Identify the blood parasite species.
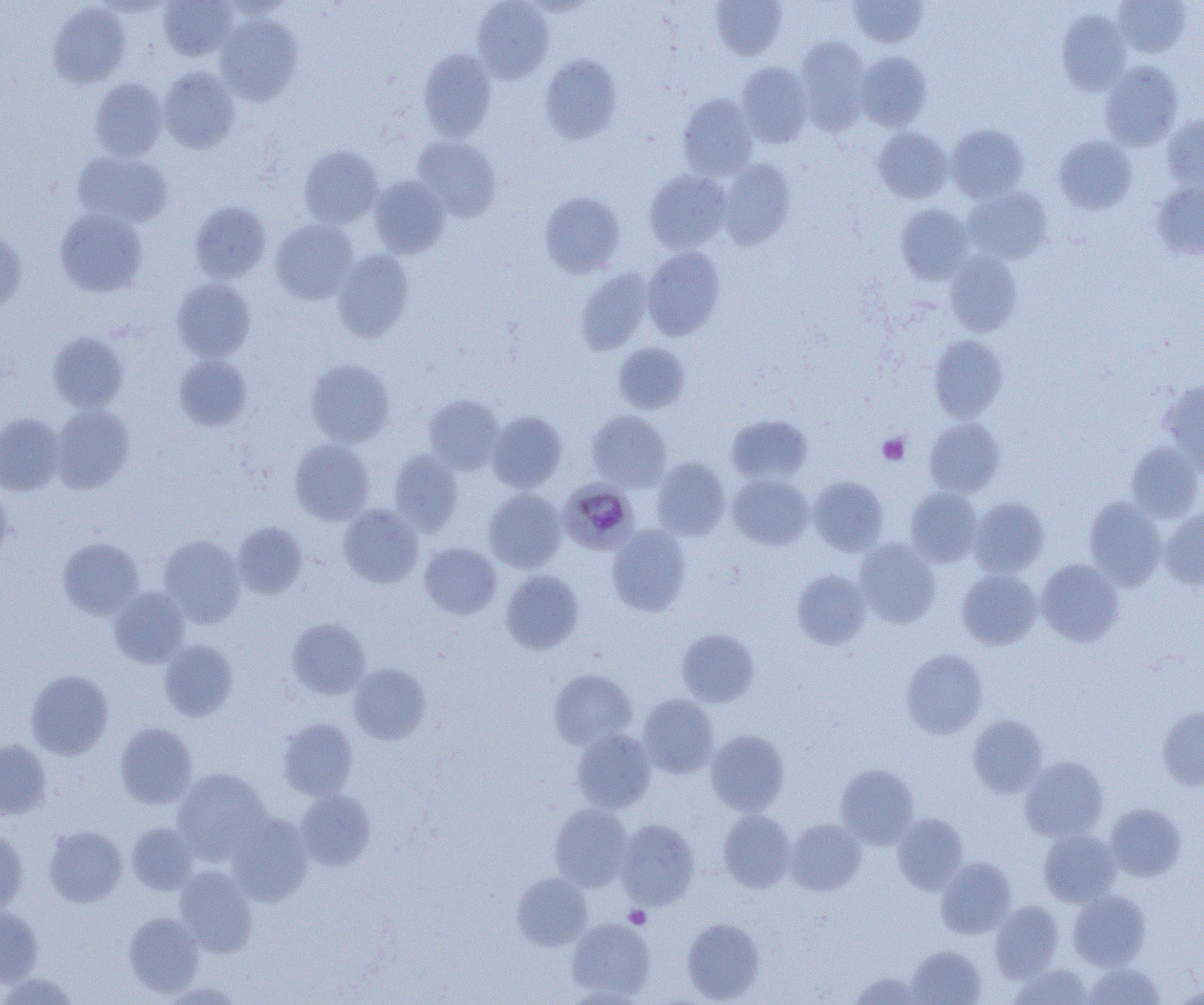

Plasmodium malariae.

Summary:
  - Coordinate format: approximate bounding boxes as (x1, y1, x2, y2) in pixels
  - Platelet locations: (877, 433, 909, 465), (624, 906, 650, 929)
  - Plasmodium malariae-infected red blood cell locations: (558, 480, 638, 554)
  - Uninfected red blood cell locations: (158, 0, 237, 61), (711, 0, 788, 60), (849, 0, 929, 48), (1111, 0, 1192, 58), (472, 1, 554, 83), (48, 3, 131, 89), (1057, 10, 1131, 95), (215, 14, 303, 104), (794, 37, 870, 135), (418, 48, 496, 141), (855, 51, 932, 131), (539, 54, 622, 144), (1100, 60, 1183, 150), (736, 62, 813, 147), (159, 68, 240, 153), (90, 78, 167, 161), (678, 93, 759, 180), (1162, 115, 1204, 191), (946, 123, 1029, 203), (872, 126, 952, 203), (1054, 135, 1137, 214), (411, 136, 502, 221), (299, 145, 383, 228), (73, 151, 173, 227), (719, 159, 796, 249), (644, 168, 732, 253), (369, 176, 450, 258), (1150, 181, 1204, 261), (963, 186, 1052, 264), (538, 191, 626, 278), (189, 200, 271, 283), (896, 203, 973, 283), (54, 208, 147, 296), (270, 219, 359, 304), (0, 228, 27, 313), (641, 246, 725, 340), (333, 250, 414, 342), (944, 251, 1023, 336), (575, 269, 652, 355), (171, 278, 256, 362), (48, 332, 128, 413), (929, 335, 1008, 422), (614, 342, 690, 414), (174, 355, 252, 431), (305, 359, 395, 447), (1160, 379, 1204, 475), (424, 393, 503, 473), (51, 404, 134, 493), (587, 410, 671, 490), (486, 411, 568, 492), (0, 413, 65, 496), (726, 414, 813, 485), (925, 418, 1004, 496), (289, 439, 375, 525), (1126, 441, 1204, 522), (389, 450, 462, 535), (651, 458, 730, 540), (727, 474, 813, 550), (808, 476, 889, 556), (0, 483, 13, 566), (905, 487, 983, 566), (484, 488, 566, 572), (1084, 496, 1167, 589), (968, 497, 1049, 577), (338, 504, 423, 587), (1160, 506, 1204, 591), (232, 522, 307, 597), (607, 525, 692, 616), (158, 535, 245, 627), (58, 537, 143, 619), (854, 538, 940, 628), (420, 543, 501, 619), (1036, 558, 1124, 646), (792, 568, 871, 649), (957, 569, 1042, 650), (500, 570, 584, 655), (109, 587, 190, 667), (286, 618, 371, 699), (677, 629, 759, 706), (159, 640, 238, 721), (901, 648, 988, 738), (349, 663, 431, 744), (549, 668, 637, 750), (26, 670, 113, 760), (638, 694, 718, 778), (1157, 706, 1204, 790), (967, 714, 1048, 797), (278, 718, 358, 800), (115, 722, 198, 808), (571, 729, 655, 812), (706, 729, 790, 815), (0, 740, 51, 820), (1019, 756, 1109, 842), (836, 764, 919, 848), (172, 768, 270, 861), (296, 790, 376, 870), (1105, 802, 1186, 881), (549, 803, 632, 890), (718, 810, 796, 892), (227, 813, 313, 905), (892, 813, 968, 894), (616, 818, 700, 909), (785, 819, 866, 895), (127, 822, 198, 894), (44, 826, 127, 907), (1039, 829, 1121, 906), (0, 830, 28, 914), (935, 857, 1016, 939), (174, 866, 258, 956), (512, 872, 592, 950), (1068, 890, 1150, 970), (990, 901, 1064, 980), (0, 905, 43, 987), (123, 911, 204, 998), (567, 918, 655, 1000), (682, 918, 765, 1003), (906, 946, 986, 1005), (1082, 962, 1165, 1005), (1010, 963, 1093, 1004), (849, 971, 927, 1004), (2, 972, 79, 1005), (563, 987, 649, 1004)
  - Field of view: single
  - Magnification: 1000x
  - Modality: light microscopy
  - Image size: 1204×1005 pixels
  - Preparation: thin blood smear